Give a bounding box for every leukocyte visible.
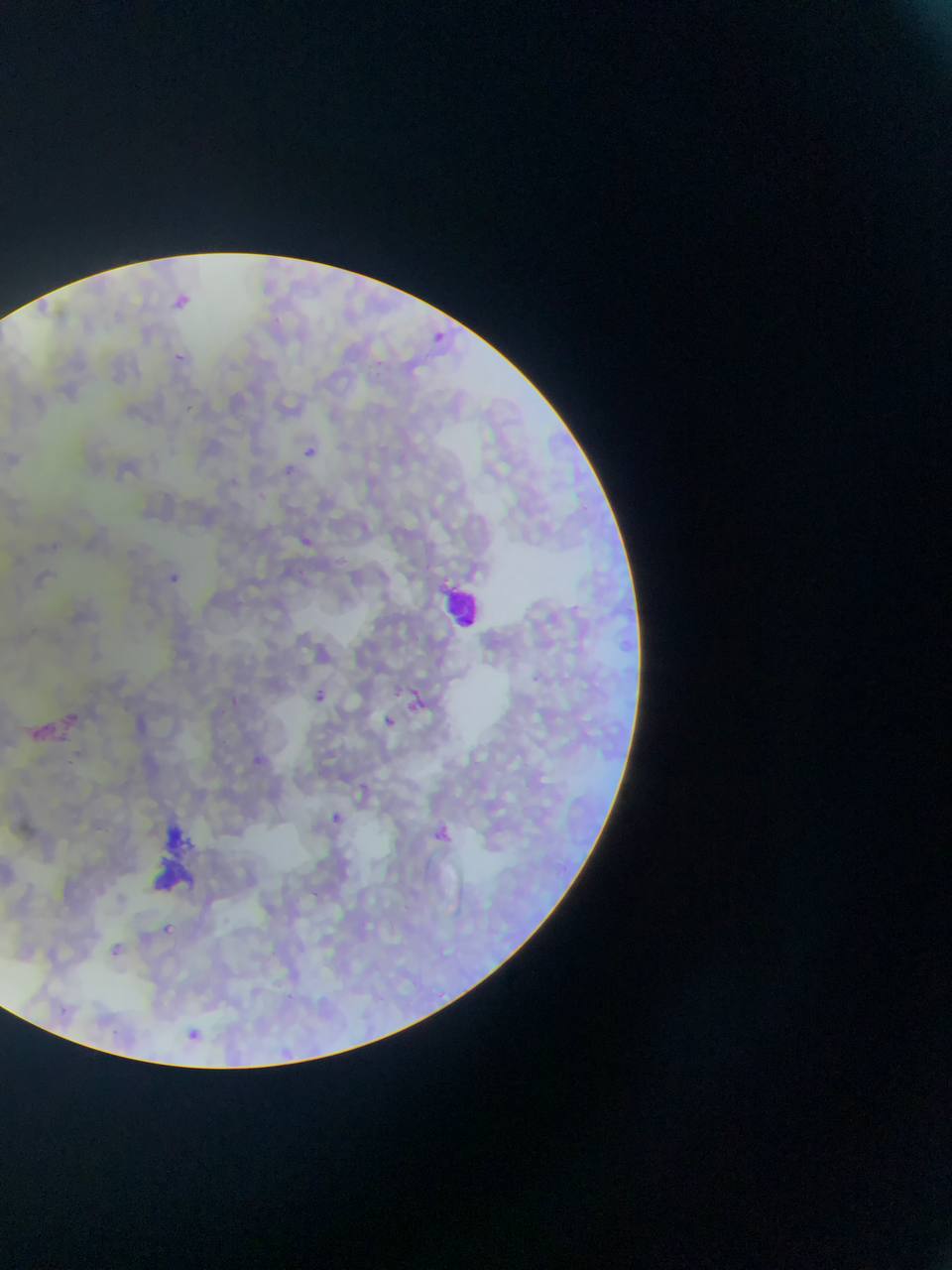

Approximate bounding boxes as left top right bottom in pixels.
Leukocytes: 446 577 484 632.

Summary:
  - Malaria parasite locations: 177 295 192 311; 434 328 448 347; 170 342 184 358; 378 359 384 368; 187 404 203 418; 302 446 324 463; 169 573 179 587; 315 690 331 707; 408 698 422 710; 383 713 402 731; 255 753 269 765; 356 779 363 787; 331 810 343 824; 434 825 460 849; 163 920 180 932; 104 941 122 957; 61 1003 68 1013; 186 1026 199 1040 | approximate x y pixel centers of objects too small to bound: 315 894
  - Artifact (stain precipitate or debris) locations: 152 806 206 895
  - Field of view: single
  - Capture: mobile-phone photograph through a microscope
  - Country: Ghana
  - Preparation: thin blood smear
  - Image size: 952×1270 pixels